Classify this cell by malaria status.
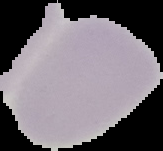
Uninfected.

Image is 163×151 pixels. From a thin blood film. The area outside the segmented cell region is set to black.